Describe the morphology of the erythrocytes.
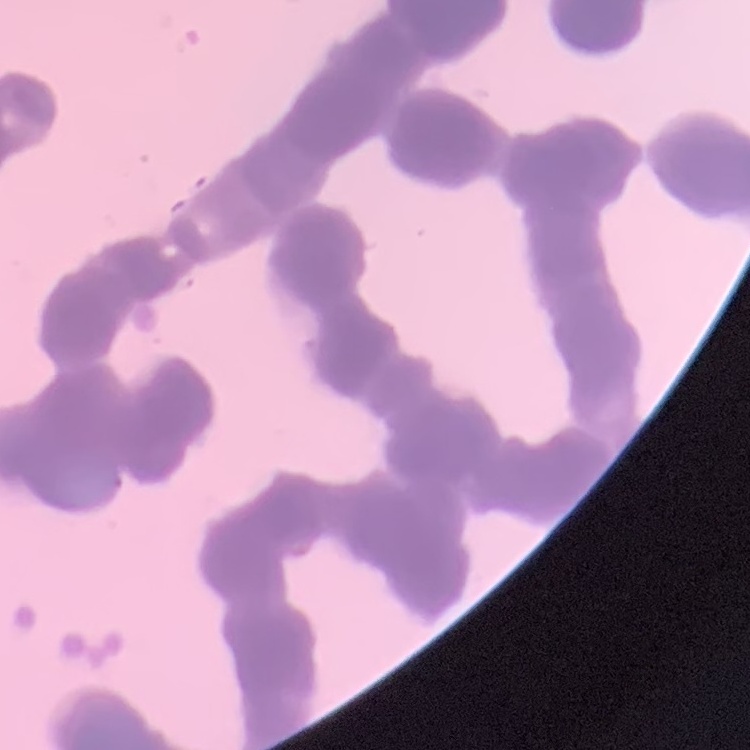

Rouleaux formation.

Thin blood smear. Square crop of a larger photomicrograph. Field's or Giemsa stain.